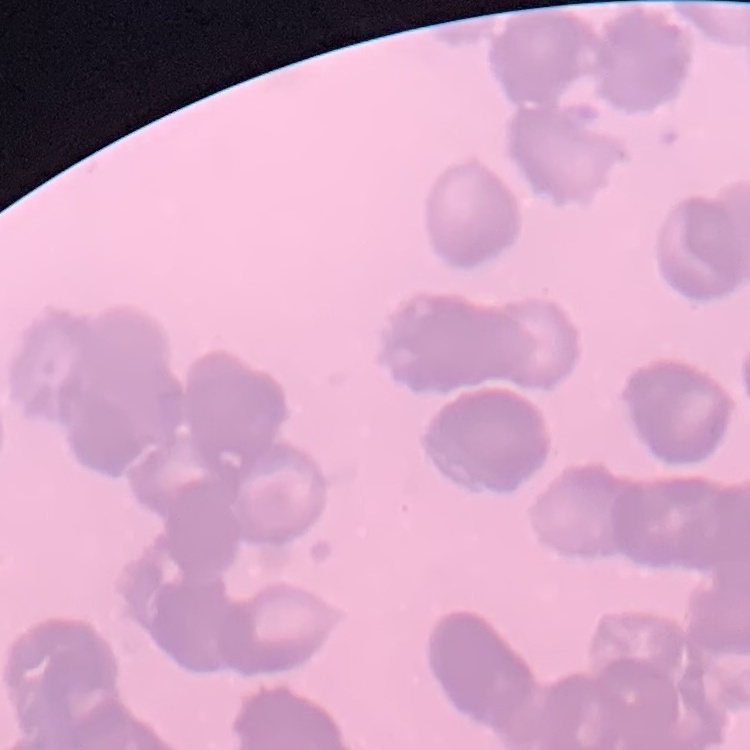
red_blood_cell_morphology: rouleaux formation
image_type: one tile cut from a larger photomicrograph
stain: Field's or Giemsa
preparation: thin peripheral smear